State which cell type is depicted.
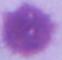

This is an erythrocyte.

magnification = 1000x
modality = photomicrograph